Give the extent of all uninfected red blood cells.
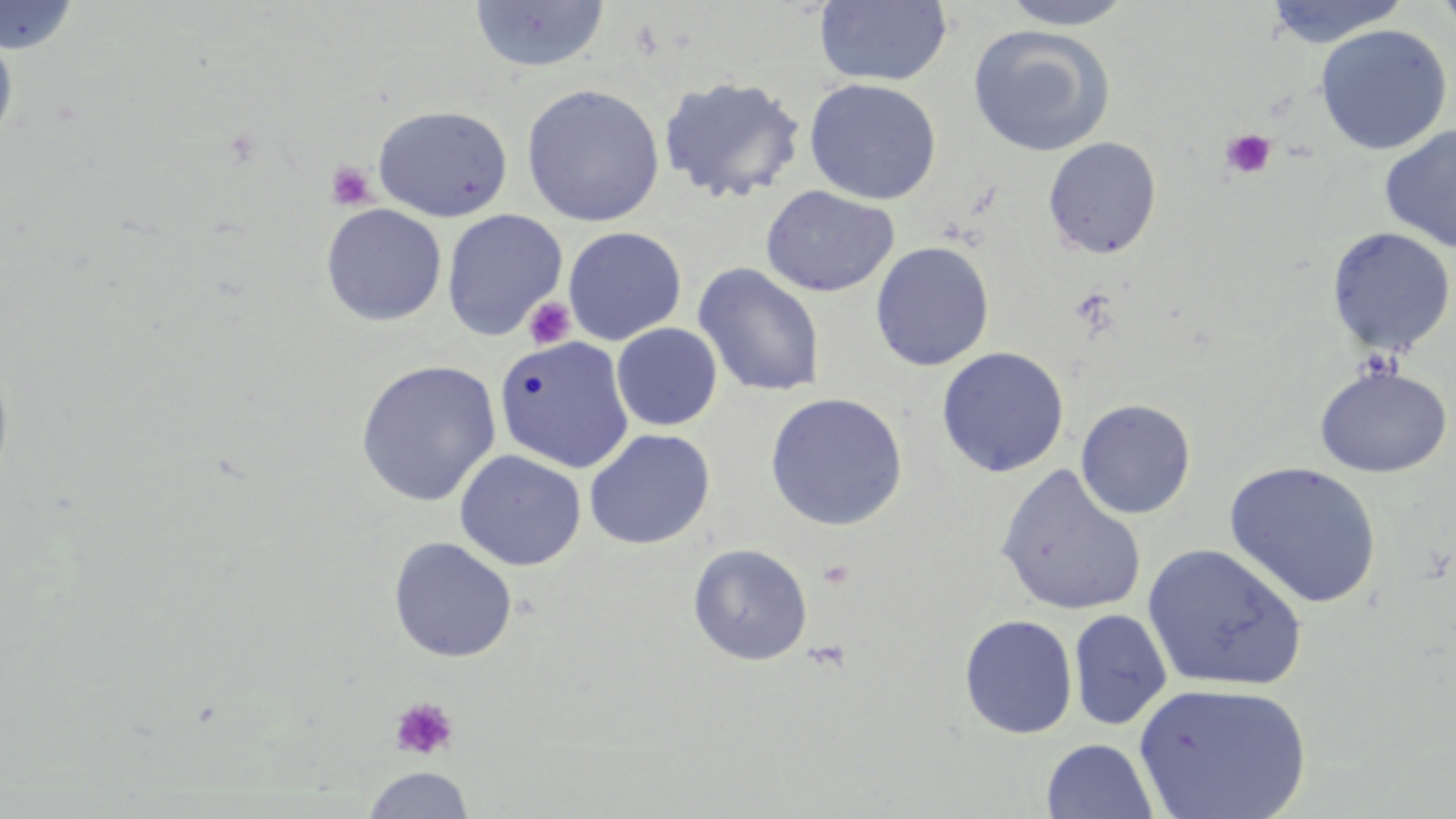

Approximate bounding boxes as (x1,y1)-(x2,y2) corner pairs in pixels.
Uninfected red blood cells: (814,0)-(953,88), (999,0)-(1134,29), (1263,0)-(1411,48), (1432,0)-(1456,37), (0,1)-(80,54), (468,1)-(611,74), (0,23)-(18,154), (967,24)-(1116,157), (1315,24)-(1453,155), (658,75)-(807,205), (804,78)-(942,205), (521,84)-(665,227), (372,104)-(513,222), (1379,124)-(1456,254), (1042,136)-(1162,259), (761,185)-(899,298), (321,203)-(447,326), (441,209)-(567,341), (563,226)-(686,345), (1326,227)-(1455,358), (870,241)-(995,371), (692,263)-(826,399), (611,323)-(723,431), (494,335)-(635,473), (936,347)-(1070,477), (0,353)-(15,492), (355,359)-(501,506), (1313,364)-(1453,478), (765,392)-(908,530), (1075,399)-(1196,520), (584,428)-(716,550), (454,449)-(587,571), (1223,461)-(1383,609), (995,465)-(1147,616), (388,537)-(517,663), (687,543)-(813,666), (1142,543)-(1308,692), (1069,609)-(1172,730), (959,614)-(1078,739), (1133,682)-(1312,819), (1041,739)-(1158,819), (361,766)-(475,818).

Platelet locations: (1220,129)-(1276,179), (326,161)-(376,209), (1069,287)-(1118,335), (523,297)-(576,349), (816,559)-(856,590), (805,639)-(851,672), (390,696)-(459,761). Slide-level diagnosis: no evidence of blood parasites. Image is 1456×819 pixels. May-Grünwald-Giemsa stain. Thin blood film. Single field of view. Optical microscopy. Captured at 1000x magnification.